Evaluate for Plasmodium parasites.
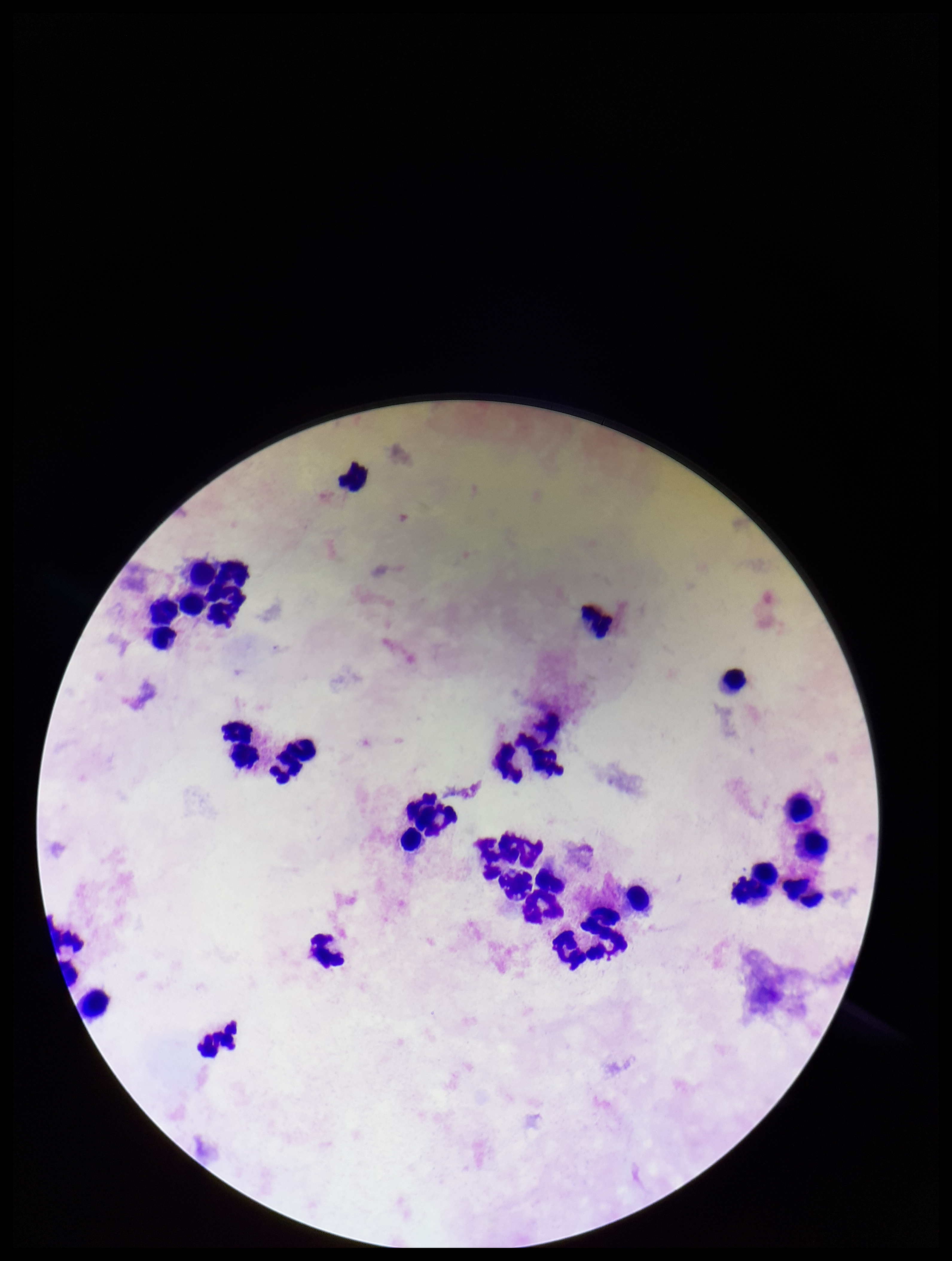

None identified.

image size = 952×1261 pixels
leukocyte count = 30
field of view = one from this slide
capture = smartphone photograph through the microscope eyepiece
preparation = thick
patient malaria status = negative
parasite count = 0
stain = Giemsa